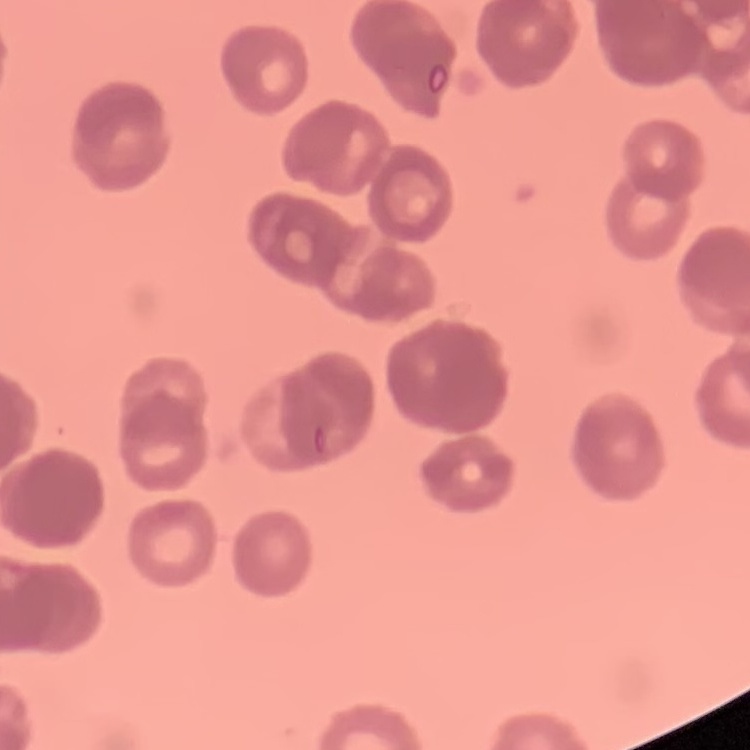

erythrocyte_morphology: rouleaux formation
preparation: thin peripheral smear
stain: Field's or Giemsa
image_type: square crop of a larger photomicrograph